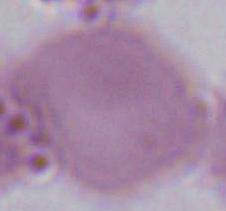

1000x magnification. An erythrocyte is seen. Micrograph.